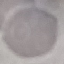

result = negative for malaria parasites
stain = Giemsa
preparation = thin blood smear
capture = smartphone through the microscope eyepiece
image type = automatically extracted cell patch, resized to 64 × 64 pixels